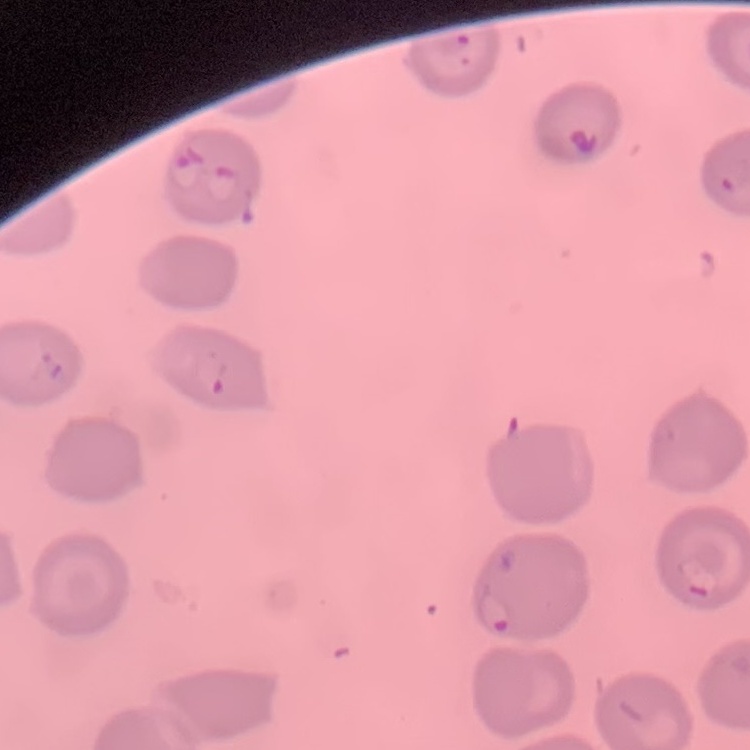
The red blood cells show no rouleaux formation. Square crop of a larger photomicrograph. Stained with either Field's or Giemsa. Thin peripheral smear.